Name the parasite shown.
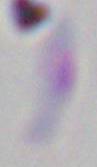
Toxoplasma gondii.

Captured at 1000x magnification. Micrograph.